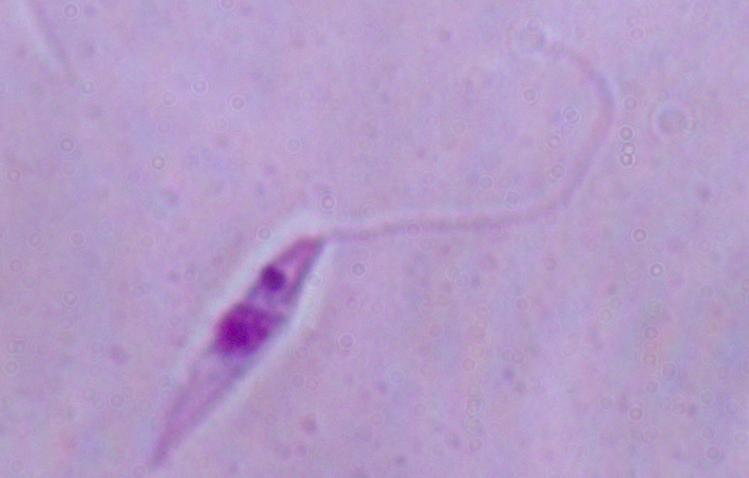
Summary:
  - Magnification: 1000x
  - Modality: photomicrograph
  - Identification: Leishmania